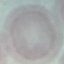
Result: no malaria parasites seen. Automatically extracted cell patch, resized to 64 × 64 pixels. Giemsa-stained preparation. Photographed with a smartphone camera at the microscope eyepiece. Thin smear of blood.